Identify the parasite.
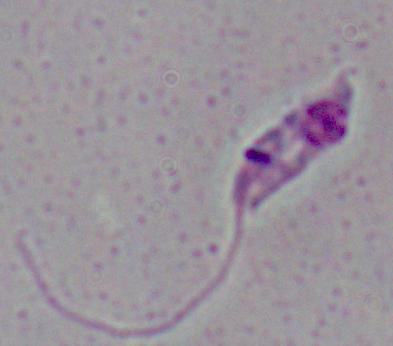
This is Leishmania.

magnification: 1000x
modality: micrograph